Give the position of each P. falciparum parasite with its life-cycle stage, each leukocyte, and any debris.
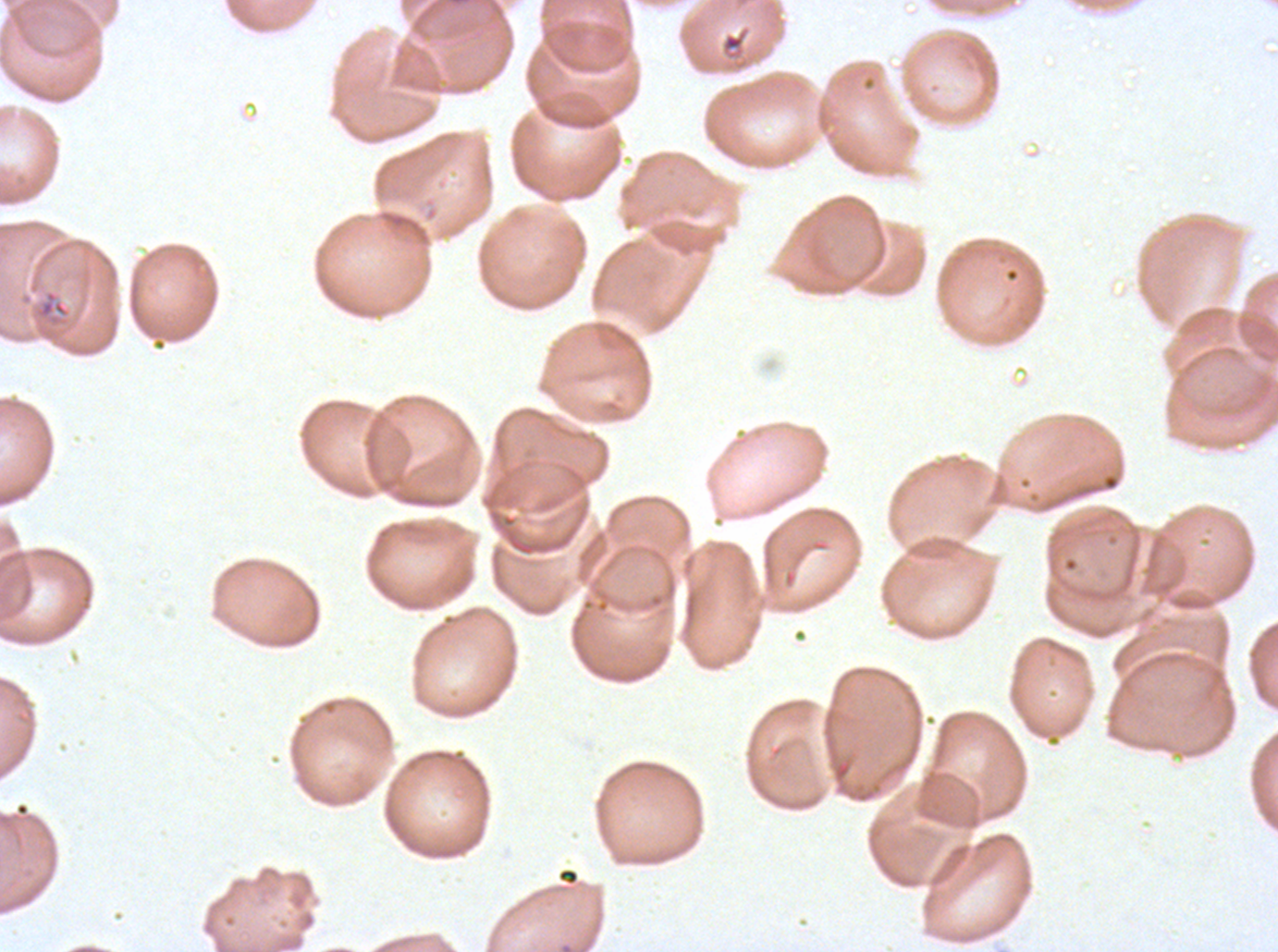
Approximate bounding boxes as {x1, y1, x2, y2} in pixels.
Debris: {720, 28, 749, 57}, {35, 289, 71, 320}.
No rings, late-ring/early-trophozoite forms, mid trophozoites, late trophozoites, early schizonts, late schizonts, segmenters, gametocytes, or leukocytes observed.

P. falciparum from a patient in The Gambia, cultured ex vivo for 24 to 48 hours. Thin blood film. One sub-image of a larger composite. Image is 1278×952 pixels. Giemsa stain.